Assess this cell for malaria.
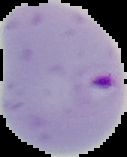
It is parasitized.

{
  "image_size": "127×157 pixels",
  "preparation": "thin blood smear",
  "image_type": "segmented cell region with the area outside set to black"
}